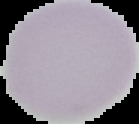

Summary:
  - Image type: cell region segmented out of the field of view; surrounding area masked to black
  - Image size: 139×124 pixels
  - Malaria status: uninfected
  - Preparation: thin blood film